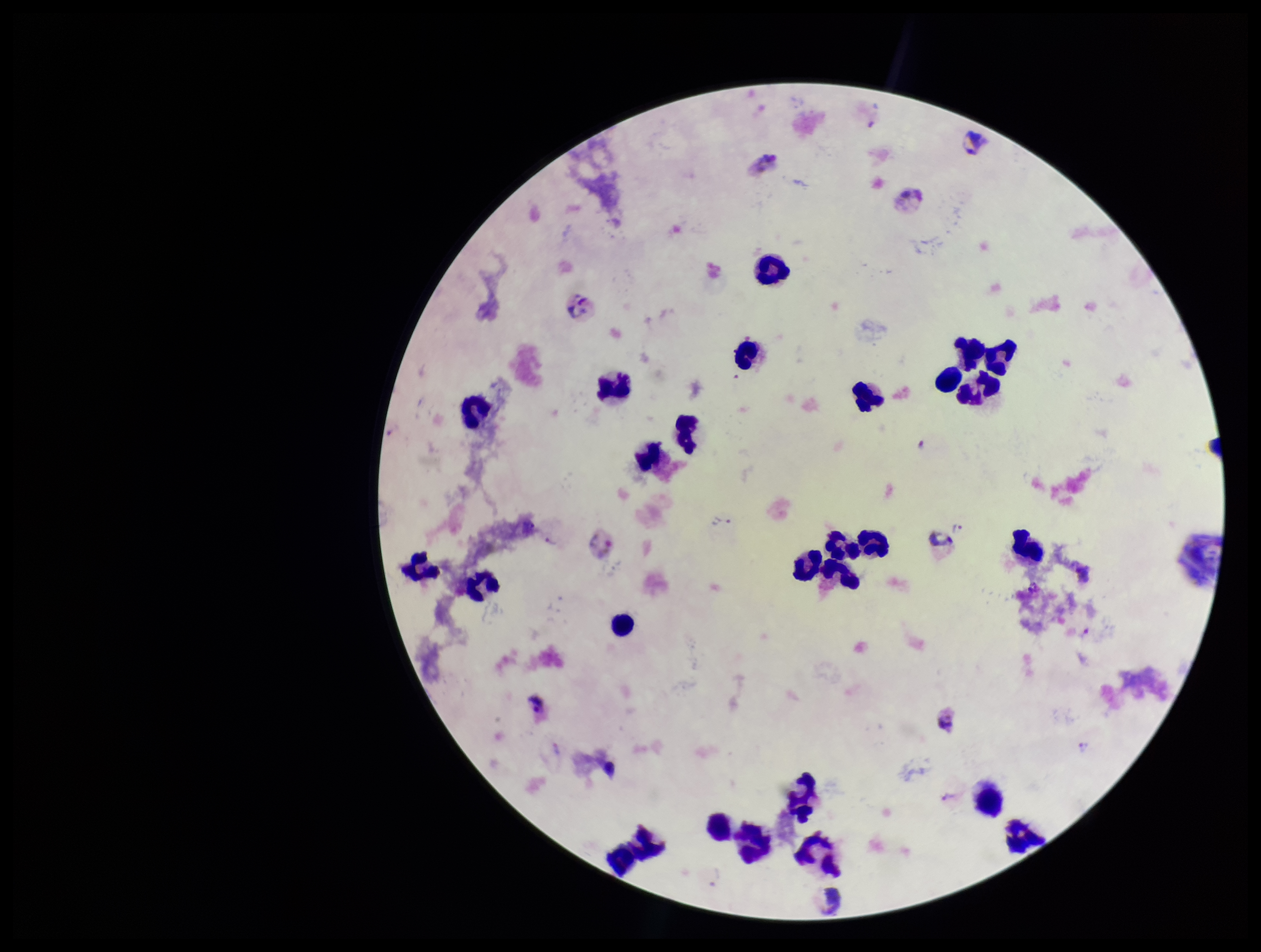
Species reported for this patient: Plasmodium vivax. Preparation: thick smear. Giemsa stain. Leukocyte count: 26. Smartphone photograph taken through the eyepiece of a microscope. Plasmodium parasites: seen. Patient malaria status: infected. Image is 1261×952 pixels. Single field of view. Parasite count: 3.